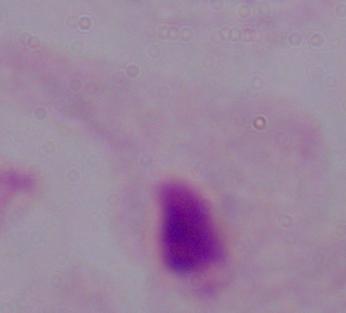
modality = photomicrograph
identification = trichomonad
magnification = 1000x